Name the cell type shown.
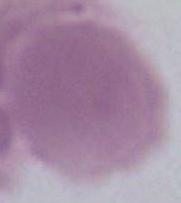
An erythrocyte.

Photomicrograph. Captured at 1000x magnification.